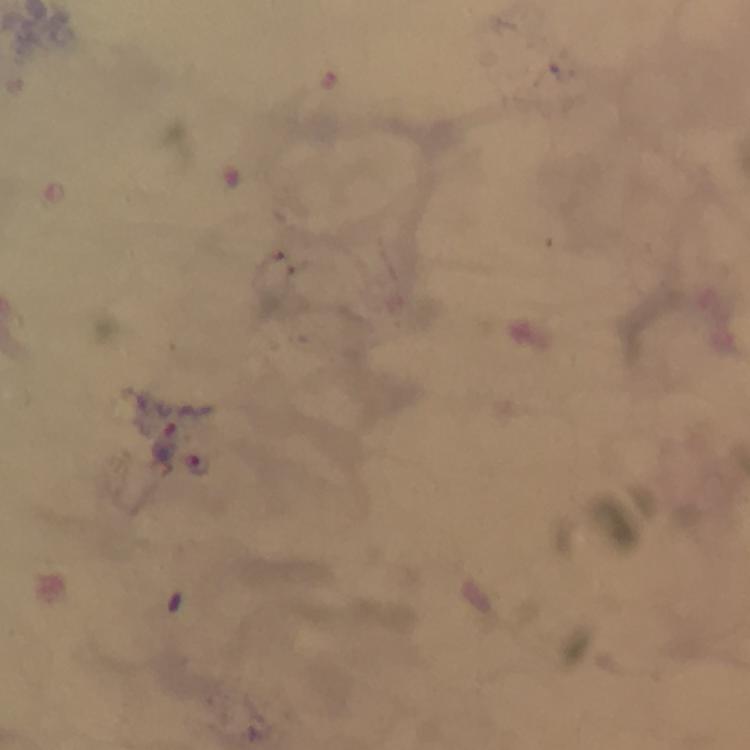
Approximate centers as {x, y} in pixels.
Summary:
  - Plasmodium parasite locations: {200, 464}
  - Magnification: 100x
  - Image size: 750×750 pixels
  - Capture: smartphone mounted on the microscope
  - Cropped from: one field of view
  - Stain: Giemsa
  - Preparation: thick blood smear
  - Context: from a diagnostic examination for malaria
  - Immersion oil: used